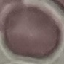
result: negative for malaria parasites
image_type: cell patch, automatically extracted from a larger field of view and resized to 64 × 64 pixels
capture: smartphone through the microscope eyepiece
stain: Giemsa
preparation: thin blood film